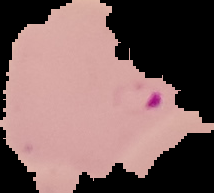

Segmented cell region on a black background. Result: Plasmodium parasites identified. Image is 214×193 pixels. From a thin blood smear.